Report the malaria status of this cell.
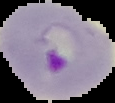

It is parasitized.

image size = 115×103 pixels
image type = segmented cell region with the area outside set to black
preparation = thin blood film